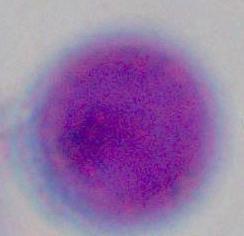

{
  "modality": "micrograph",
  "magnification": "1000x",
  "identification": "leukocyte"
}